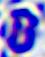
Summary:
  - Modality: micrograph
  - Identification: white blood cell
  - Magnification: 400x